Classify this cell by malaria status.
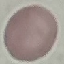
It is uninfected.

Thin blood smear. Automatically extracted cell patch, resized to 64 × 64 pixels. Acquired by smartphone through the microscope eyepiece. Giemsa-stained preparation.